Identify the cell.
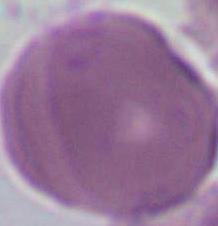

An erythrocyte.

Summary:
  - Modality: micrograph
  - Magnification: 1000x